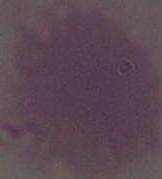
1000x magnification. Micrograph. A red blood cell is seen.